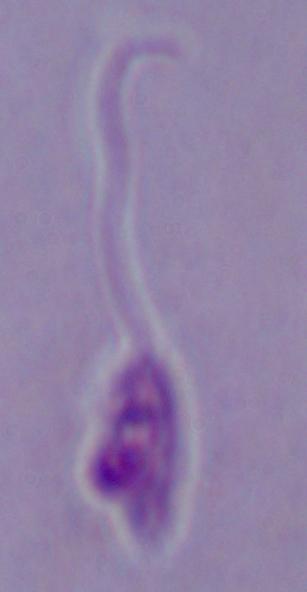

{
  "modality": "photomicrograph",
  "magnification": "1000x",
  "identification": "Leishmania"
}